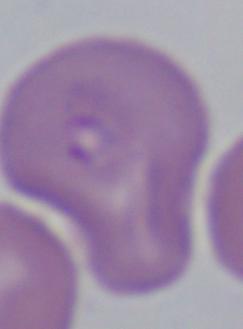
magnification = 1000x
modality = micrograph
identification = Babesia